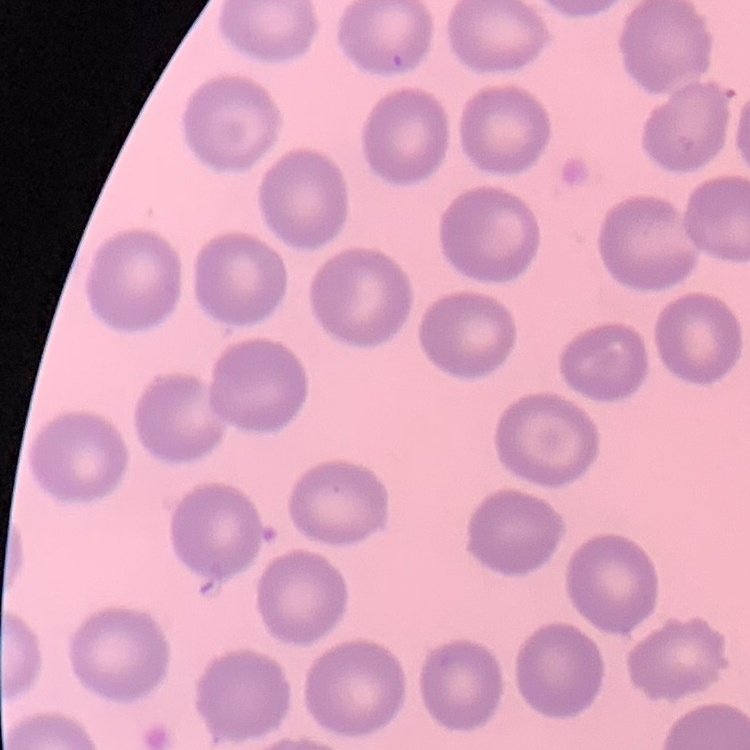

red_blood_cell_morphology: no rouleaux formation
image_type: one tile cut from a larger photomicrograph
stain: Field's or Giemsa
preparation: thin blood film